State which parasite is depicted.
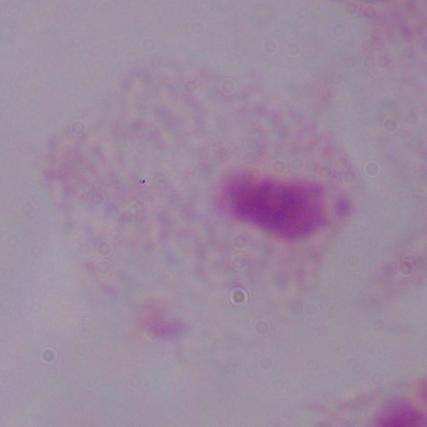
A trichomonad.

{
  "magnification": "1000x",
  "modality": "micrograph"
}